Identify the blood parasite species.
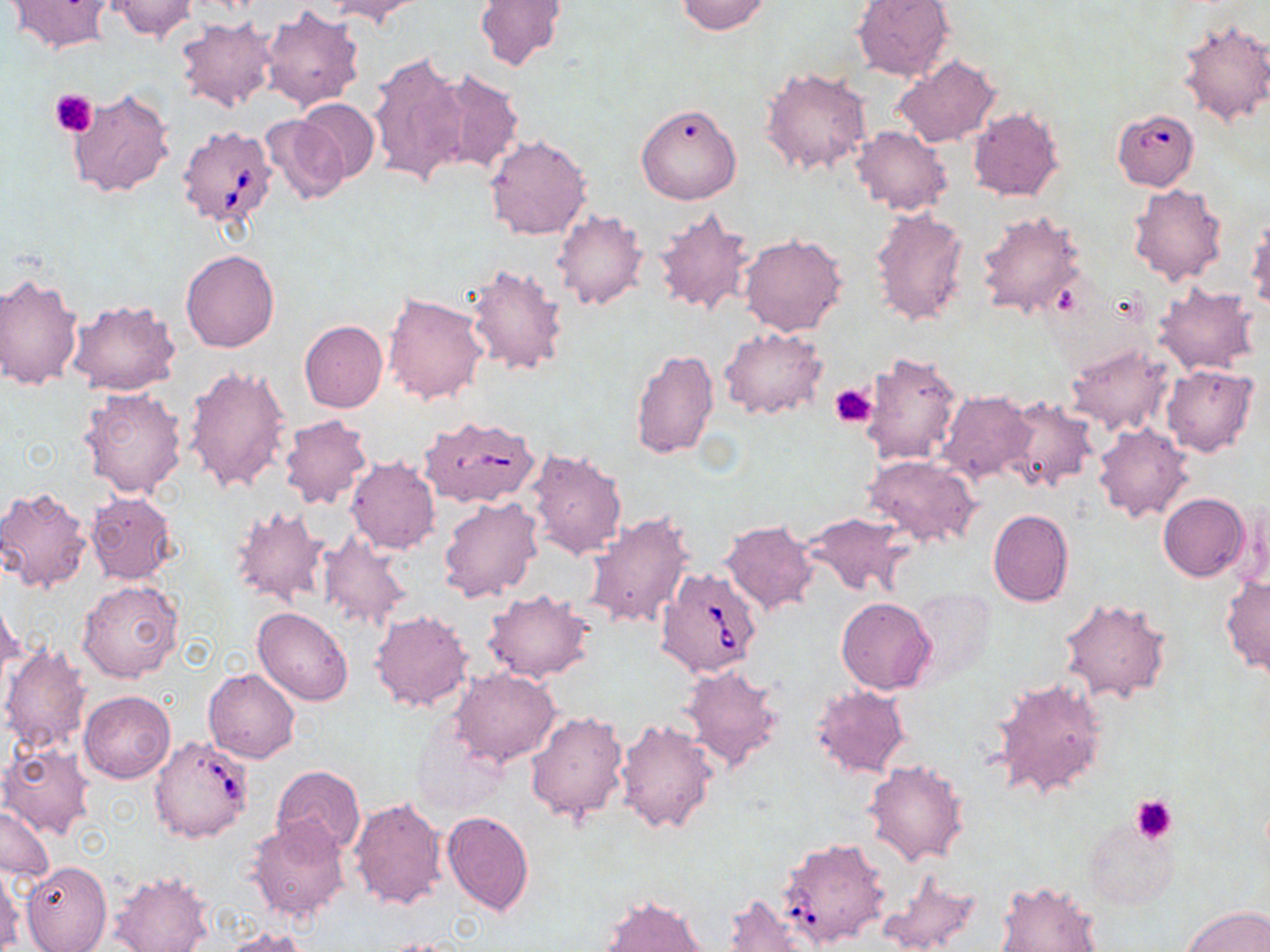
Babesia divergens.

image size = 1270×952 pixels
uninfected red blood cell locations = approximate bounding boxes as (x1, y1, x2, y2) in pixels: (6, 0, 117, 52), (110, 0, 195, 43), (675, 0, 771, 35), (851, 0, 955, 81), (325, 1, 428, 27), (474, 1, 566, 71), (259, 4, 364, 111), (176, 16, 280, 113), (1177, 18, 1270, 127), (368, 50, 472, 190), (892, 54, 1001, 149), (760, 66, 873, 176), (430, 69, 524, 177), (65, 86, 176, 199), (295, 98, 379, 184), (636, 102, 742, 204), (968, 108, 1064, 201), (261, 115, 350, 204), (850, 125, 952, 216), (483, 134, 591, 241), (1129, 183, 1228, 287), (653, 205, 757, 318), (869, 206, 970, 327), (976, 209, 1086, 321), (552, 210, 648, 311), (1246, 217, 1270, 314), (738, 232, 849, 337), (180, 248, 280, 352), (464, 261, 571, 376), (0, 273, 83, 390), (1153, 282, 1262, 376), (382, 291, 488, 405), (65, 299, 179, 396), (299, 320, 388, 414), (718, 326, 826, 421), (1063, 341, 1175, 437), (630, 348, 719, 460), (860, 349, 964, 466), (184, 364, 291, 494), (1161, 364, 1259, 457), (78, 387, 189, 498), (938, 391, 1033, 484), (1001, 397, 1097, 494), (279, 415, 372, 510), (1093, 423, 1194, 523), (525, 445, 629, 559), (864, 455, 982, 548), (346, 457, 440, 555), (0, 486, 92, 593), (86, 492, 177, 584), (1159, 493, 1249, 581), (437, 495, 544, 604), (228, 503, 332, 608), (987, 509, 1074, 607), (583, 510, 697, 629), (803, 511, 913, 598), (721, 519, 819, 614), (317, 530, 413, 632), (1220, 575, 1270, 675), (78, 579, 185, 683), (907, 586, 995, 686), (483, 590, 593, 684), (0, 595, 23, 688), (1058, 596, 1172, 704), (836, 597, 935, 694), (253, 608, 355, 705), (370, 609, 473, 712), (2, 640, 91, 756), (681, 664, 785, 775), (203, 668, 300, 763), (452, 668, 559, 767), (991, 676, 1110, 801), (811, 684, 910, 778), (80, 690, 175, 783), (526, 711, 629, 823), (407, 716, 507, 820), (614, 718, 719, 836), (1, 745, 94, 839), (863, 759, 970, 867), (272, 764, 365, 857), (349, 798, 447, 910), (1, 804, 54, 883), (441, 810, 534, 916), (1080, 815, 1179, 912), (246, 818, 350, 923), (20, 860, 111, 952), (0, 864, 22, 949), (875, 868, 981, 952), (109, 871, 214, 952), (996, 880, 1103, 952), (724, 892, 817, 951), (598, 894, 709, 952), (1183, 905, 1270, 951), (217, 927, 312, 952), (378, 937, 473, 952)
modality = light microscopy
stain = May-Grünwald-Giemsa
Babesia divergens-infected red blood cell locations = approximate bounding boxes as (x1, y1, x2, y2) in pixels: (1112, 108, 1199, 190), (177, 125, 278, 228), (420, 416, 540, 508), (655, 568, 762, 676), (149, 735, 253, 842), (778, 836, 892, 950)
preparation = thin blood smear
magnification = 1000x
field of view = one of a larger specimen
platelet locations = approximate bounding boxes as (x1, y1, x2, y2) in pixels: (50, 89, 97, 137), (830, 384, 875, 427), (1130, 794, 1178, 843)